Comment on the morphology of the red blood cells.
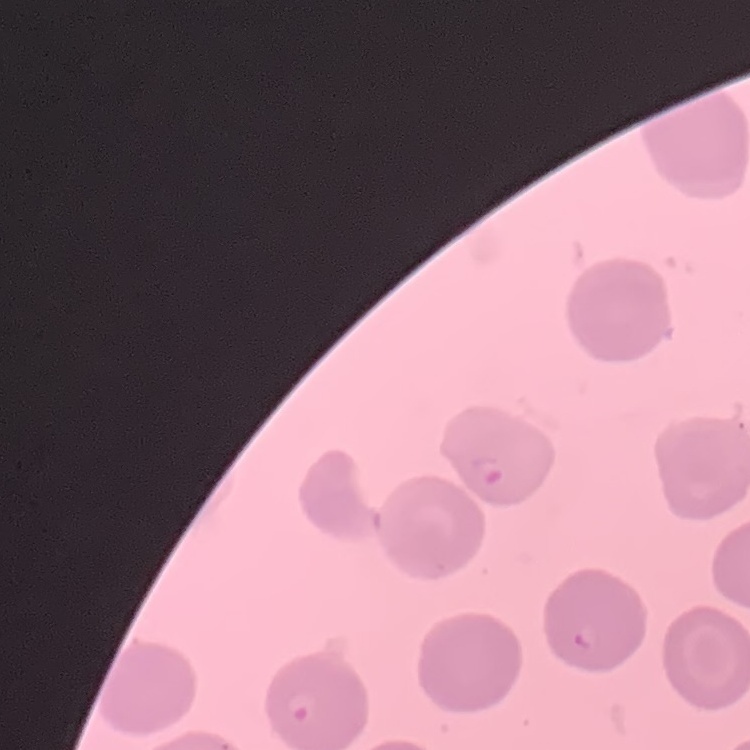
No rouleaux formation.

Summary:
  - Preparation: thin blood film
  - Stain: Field's or Giemsa
  - Image type: one tile cut from a larger photomicrograph